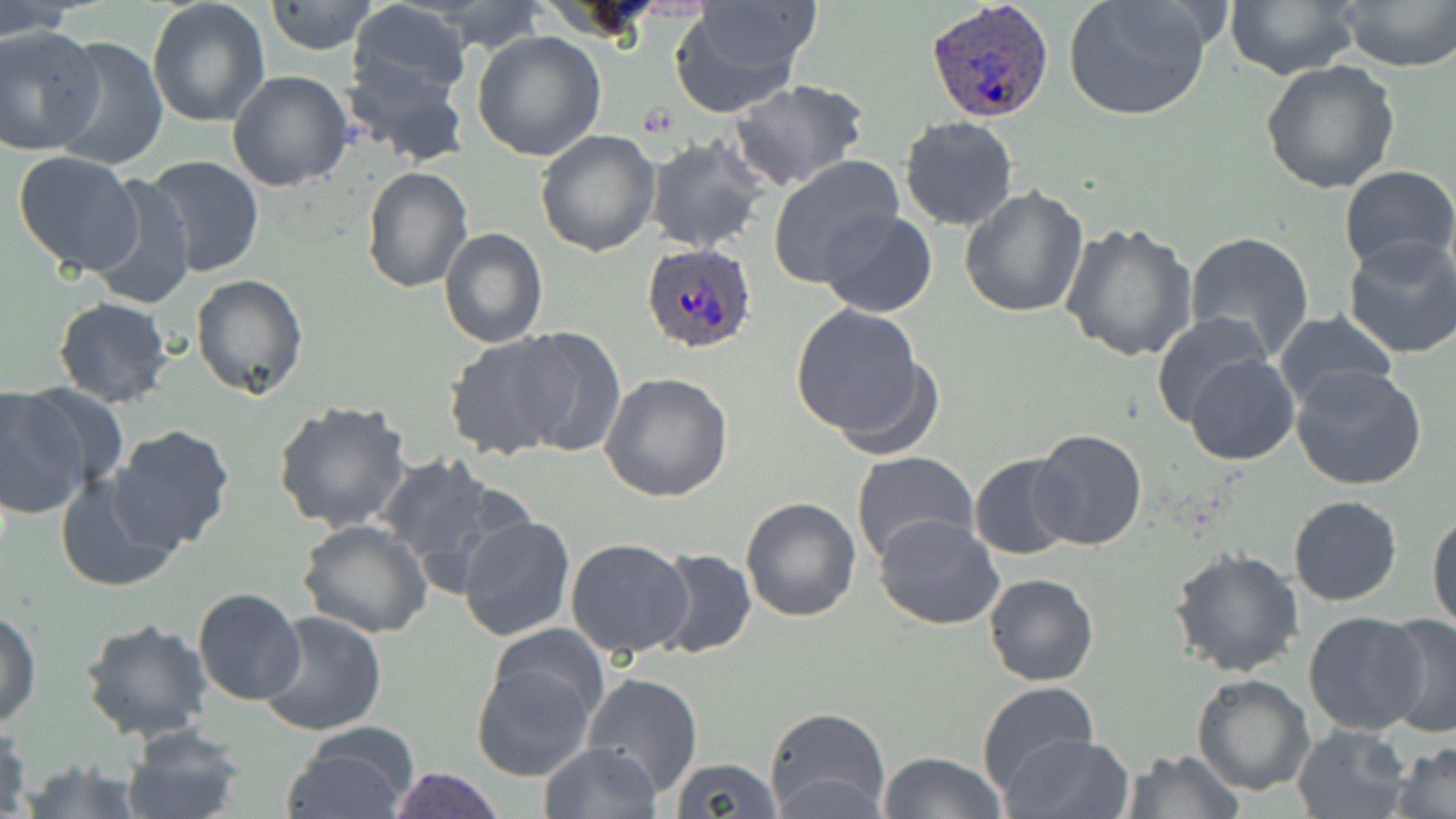
Approximate bounding boxes as named x1/y1/x2/y2 corners in pixels. Platelet locations: (x1=638, y1=103, x2=681, y2=139). Uninfected red blood cell locations: (x1=267, y1=0, x2=377, y2=55), (x1=347, y1=0, x2=473, y2=103), (x1=1063, y1=0, x2=1215, y2=122), (x1=1226, y1=0, x2=1363, y2=80), (x1=1337, y1=0, x2=1455, y2=71), (x1=425, y1=1, x2=550, y2=53), (x1=669, y1=1, x2=818, y2=112), (x1=148, y1=2, x2=272, y2=127), (x1=0, y1=3, x2=79, y2=40), (x1=0, y1=26, x2=102, y2=155), (x1=472, y1=30, x2=606, y2=160), (x1=48, y1=35, x2=168, y2=171), (x1=342, y1=58, x2=468, y2=169), (x1=1260, y1=60, x2=1400, y2=194), (x1=226, y1=71, x2=354, y2=191), (x1=729, y1=78, x2=870, y2=191), (x1=898, y1=116, x2=1020, y2=232), (x1=534, y1=130, x2=661, y2=257), (x1=644, y1=135, x2=771, y2=253), (x1=12, y1=151, x2=145, y2=276), (x1=767, y1=155, x2=907, y2=288), (x1=144, y1=157, x2=265, y2=277), (x1=1337, y1=165, x2=1455, y2=277), (x1=362, y1=166, x2=473, y2=294), (x1=86, y1=175, x2=197, y2=310), (x1=959, y1=184, x2=1091, y2=321), (x1=817, y1=208, x2=938, y2=317), (x1=1061, y1=223, x2=1197, y2=363), (x1=439, y1=226, x2=549, y2=348), (x1=1184, y1=231, x2=1315, y2=362), (x1=1342, y1=237, x2=1456, y2=359), (x1=189, y1=273, x2=308, y2=399), (x1=51, y1=296, x2=176, y2=409), (x1=790, y1=303, x2=932, y2=447), (x1=1272, y1=308, x2=1396, y2=410), (x1=1150, y1=310, x2=1273, y2=429), (x1=508, y1=326, x2=625, y2=456), (x1=444, y1=333, x2=573, y2=460), (x1=1185, y1=353, x2=1299, y2=466), (x1=1291, y1=366, x2=1428, y2=490), (x1=599, y1=373, x2=733, y2=503), (x1=21, y1=382, x2=128, y2=493), (x1=0, y1=385, x2=89, y2=519), (x1=272, y1=399, x2=413, y2=533), (x1=108, y1=424, x2=238, y2=553), (x1=1029, y1=428, x2=1146, y2=551), (x1=850, y1=451, x2=980, y2=567), (x1=380, y1=453, x2=510, y2=589), (x1=969, y1=454, x2=1077, y2=561), (x1=53, y1=471, x2=184, y2=592), (x1=740, y1=496, x2=861, y2=621), (x1=1287, y1=496, x2=1402, y2=607), (x1=1428, y1=507, x2=1456, y2=634), (x1=874, y1=513, x2=1004, y2=629), (x1=457, y1=516, x2=576, y2=642), (x1=298, y1=520, x2=432, y2=639), (x1=565, y1=537, x2=694, y2=659), (x1=1169, y1=547, x2=1305, y2=679), (x1=651, y1=548, x2=757, y2=661), (x1=983, y1=573, x2=1099, y2=685), (x1=191, y1=587, x2=306, y2=707), (x1=1, y1=610, x2=42, y2=727), (x1=1303, y1=610, x2=1431, y2=736), (x1=255, y1=611, x2=387, y2=736), (x1=1378, y1=613, x2=1456, y2=739), (x1=79, y1=617, x2=213, y2=744), (x1=484, y1=623, x2=612, y2=733), (x1=470, y1=661, x2=595, y2=781), (x1=583, y1=672, x2=703, y2=795), (x1=1191, y1=674, x2=1314, y2=796), (x1=976, y1=682, x2=1100, y2=795), (x1=764, y1=707, x2=890, y2=819), (x1=0, y1=723, x2=32, y2=819), (x1=1290, y1=723, x2=1413, y2=819), (x1=121, y1=726, x2=250, y2=819), (x1=281, y1=730, x2=418, y2=819), (x1=1004, y1=734, x2=1133, y2=819), (x1=538, y1=741, x2=661, y2=819), (x1=1391, y1=741, x2=1456, y2=819), (x1=1123, y1=748, x2=1242, y2=818), (x1=879, y1=751, x2=1005, y2=819), (x1=18, y1=757, x2=145, y2=819), (x1=670, y1=757, x2=783, y2=819), (x1=386, y1=766, x2=506, y2=819). Plasmodium ovale-infected red blood cell locations: (x1=927, y1=0, x2=1056, y2=123), (x1=639, y1=243, x2=758, y2=353). Slide-level diagnosis: Plasmodium ovale. Optical microscopy. May-Grünwald-Giemsa-stained preparation. Thin blood film. 1000x magnification. Image is 1456×819 pixels. One field of a larger specimen.